Report the malaria status of this cell.
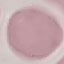

It is uninfected.

stain = Giemsa
image type = automatically extracted cell patch, resized to 64 × 64 pixels
preparation = thin smear
capture = smartphone through the microscope eyepiece